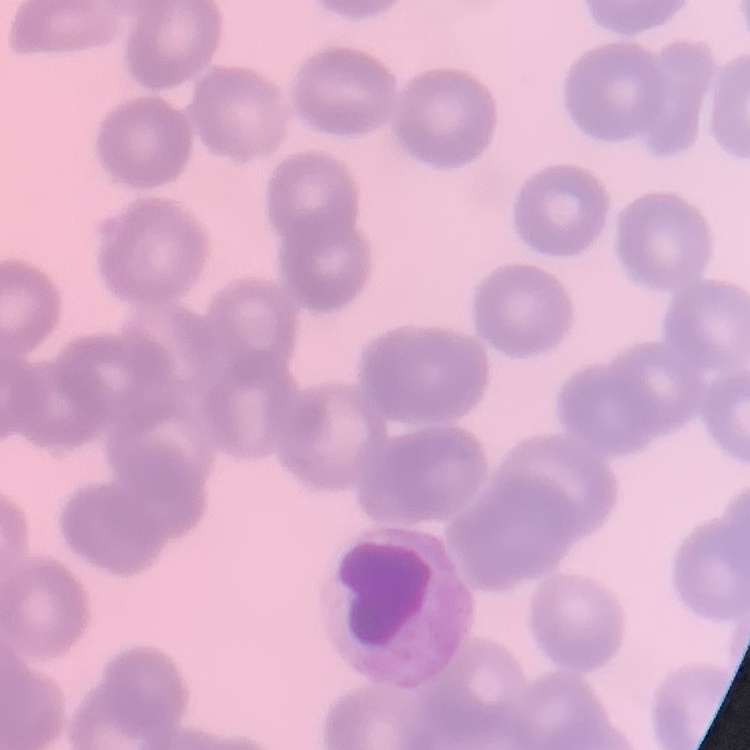

The red blood cells exhibit no rouleaux formation. Thin blood film. One tile cut from a larger photomicrograph. Field's or Giemsa stain.